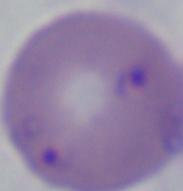
magnification: 1000x
identification: Babesia
modality: photomicrograph